State the blood parasite species.
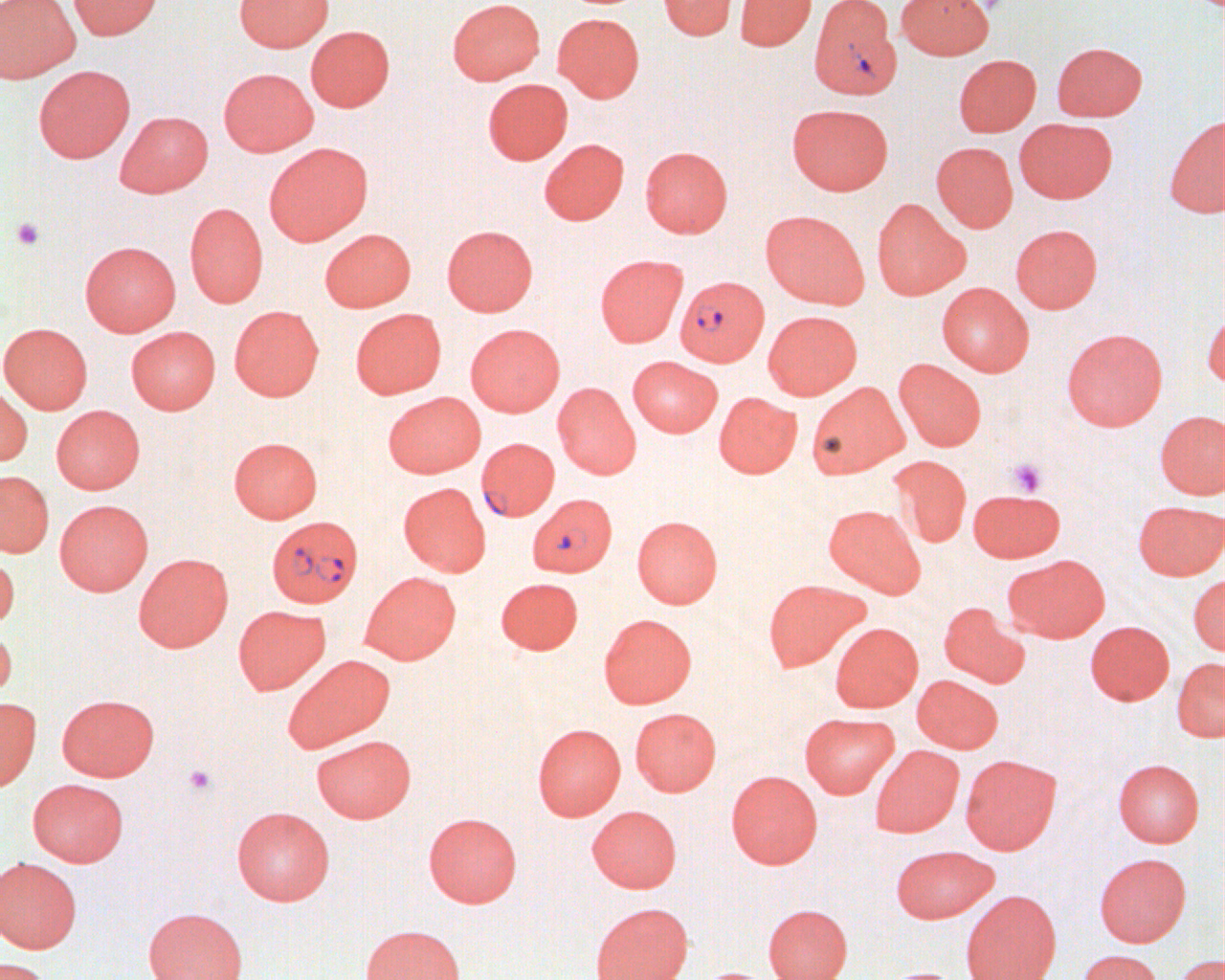

Plasmodium falciparum.

modality = optical microscopy
magnification = 1000x
Plasmodium falciparum-infected red blood cell locations = approximate bounding boxes as (x1, y1, x2, y2) in pixels: (808, 0, 902, 99), (675, 275, 769, 367), (476, 438, 559, 522), (528, 493, 617, 577), (267, 515, 362, 607)
platelet locations = approximate bounding boxes as (x1, y1, x2, y2) in pixels: (11, 217, 45, 250), (1008, 459, 1046, 496), (185, 765, 216, 795)
image size = 1225×980 pixels
uninfected red blood cell locations = approximate bounding boxes as (x1, y1, x2, y2) in pixels: (0, 0, 79, 82), (68, 0, 162, 39), (234, 0, 333, 51), (447, 0, 544, 85), (659, 0, 736, 40), (735, 0, 816, 50), (896, 0, 994, 59), (553, 13, 644, 102), (305, 25, 395, 112), (1052, 41, 1147, 121), (954, 54, 1041, 137), (33, 64, 136, 163), (218, 68, 319, 156), (482, 78, 573, 165), (787, 103, 892, 195), (115, 110, 213, 197), (1164, 116, 1225, 218), (1014, 118, 1116, 203), (539, 138, 629, 225), (265, 142, 373, 245), (931, 142, 1018, 232), (640, 145, 732, 237), (871, 198, 968, 300), (184, 202, 268, 307), (761, 210, 869, 308), (1011, 223, 1102, 313), (441, 224, 537, 315), (320, 228, 416, 312), (80, 241, 181, 336), (594, 254, 687, 347), (936, 282, 1033, 376), (229, 305, 324, 400), (350, 309, 446, 398), (763, 310, 862, 399), (1201, 311, 1225, 390), (0, 323, 92, 413), (465, 323, 565, 416), (126, 326, 220, 414), (1061, 328, 1167, 431), (627, 355, 722, 437), (893, 358, 986, 451), (806, 381, 907, 479), (553, 382, 641, 479), (0, 384, 33, 466), (383, 391, 485, 477), (714, 392, 801, 478), (51, 405, 144, 494), (1154, 410, 1225, 499), (228, 437, 323, 523), (888, 455, 972, 548), (0, 471, 54, 556), (398, 482, 490, 576), (967, 488, 1065, 562), (54, 499, 153, 595), (1133, 500, 1225, 580), (823, 504, 925, 597), (632, 515, 723, 608), (0, 553, 20, 630), (134, 553, 233, 652), (1004, 554, 1110, 642), (360, 571, 461, 664), (1188, 573, 1225, 656), (496, 578, 582, 654), (762, 578, 869, 672), (938, 602, 1030, 687), (233, 605, 330, 695), (598, 613, 696, 709), (1085, 620, 1174, 705), (830, 622, 923, 712), (0, 627, 17, 702), (283, 654, 394, 753), (1171, 657, 1225, 741), (912, 674, 1003, 753), (57, 694, 159, 781), (0, 697, 41, 790), (630, 707, 721, 796), (799, 712, 899, 798), (532, 723, 626, 820), (310, 734, 417, 823), (870, 745, 963, 837), (960, 754, 1061, 854), (1113, 758, 1204, 847), (726, 770, 822, 868), (27, 778, 128, 866), (587, 805, 682, 892), (231, 806, 335, 905), (423, 812, 522, 907), (890, 844, 999, 923), (1093, 852, 1191, 947), (0, 857, 82, 953), (961, 889, 1061, 980), (591, 902, 693, 980), (763, 903, 853, 980), (143, 906, 247, 980), (361, 924, 465, 980), (1075, 949, 1164, 980), (1174, 954, 1225, 980), (0, 957, 50, 980), (879, 966, 966, 980), (694, 967, 777, 980)
preparation = thin blood smear
field of view = single